Locate platelets.
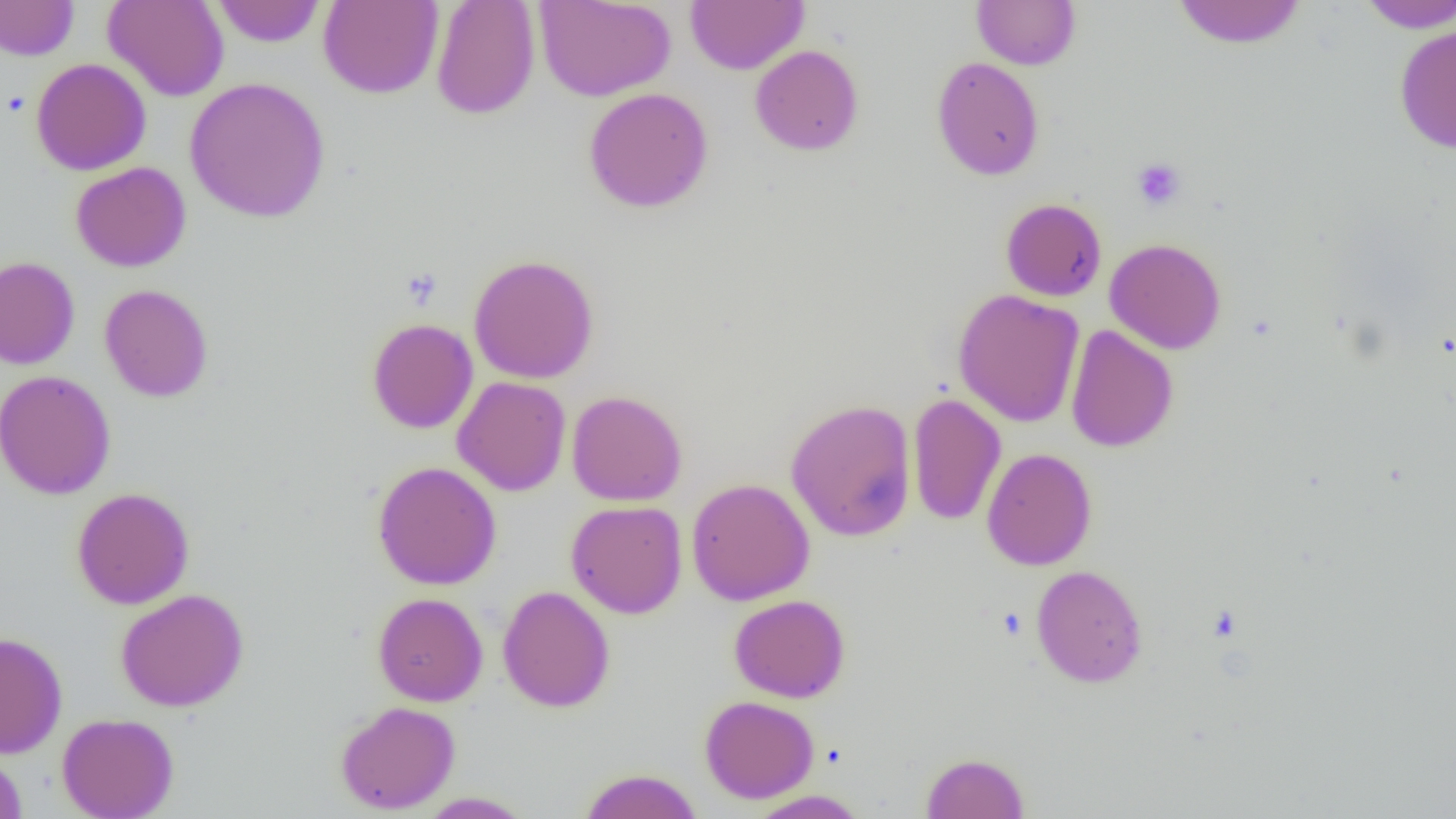
Approximate bounding boxes as (x1, y1, x2, y2) in pixels.
Platelets: (2, 92, 30, 118), (1132, 158, 1186, 210), (401, 268, 443, 309).

Uninfected red blood cell locations: (103, 0, 229, 101), (212, 0, 325, 47), (318, 0, 443, 98), (431, 0, 540, 119), (534, 0, 676, 101), (686, 0, 808, 74), (971, 0, 1081, 70), (1355, 0, 1456, 33), (0, 1, 78, 60), (1172, 1, 1307, 48), (1394, 24, 1456, 153), (750, 44, 864, 155), (931, 56, 1045, 180), (31, 58, 151, 176), (184, 77, 331, 223), (584, 87, 714, 213), (70, 162, 191, 272), (1001, 198, 1107, 301), (1105, 238, 1227, 354), (468, 254, 600, 384), (0, 256, 80, 370), (0, 256, 89, 497), (99, 284, 214, 402), (953, 289, 1085, 427), (366, 318, 478, 434), (1065, 324, 1178, 452), (0, 370, 116, 500), (453, 376, 571, 496), (567, 390, 687, 506), (908, 392, 1006, 526), (785, 398, 917, 541), (982, 447, 1097, 570), (372, 461, 502, 590), (686, 478, 815, 605), (71, 487, 195, 609), (566, 500, 687, 619), (1032, 565, 1148, 688), (497, 585, 616, 712), (115, 588, 249, 711), (372, 592, 488, 706), (729, 594, 850, 703), (0, 631, 68, 758), (699, 695, 819, 803), (335, 701, 460, 814), (57, 713, 179, 819), (0, 750, 27, 818), (921, 752, 1029, 818), (578, 768, 703, 819), (746, 790, 870, 818), (417, 792, 533, 818). Slide-level diagnosis: negative for blood parasites. Image is 1456×819 pixels. Thin blood smear. Captured at 1000x magnification. Single field of view. Optical microscopy.